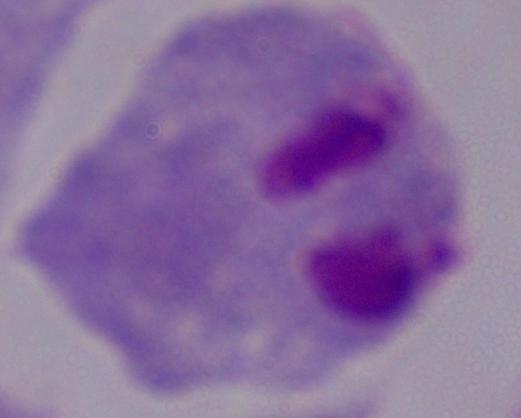
{
  "identification": "trichomonad",
  "modality": "micrograph",
  "magnification": "1000x"
}